Point out each malaria parasite.
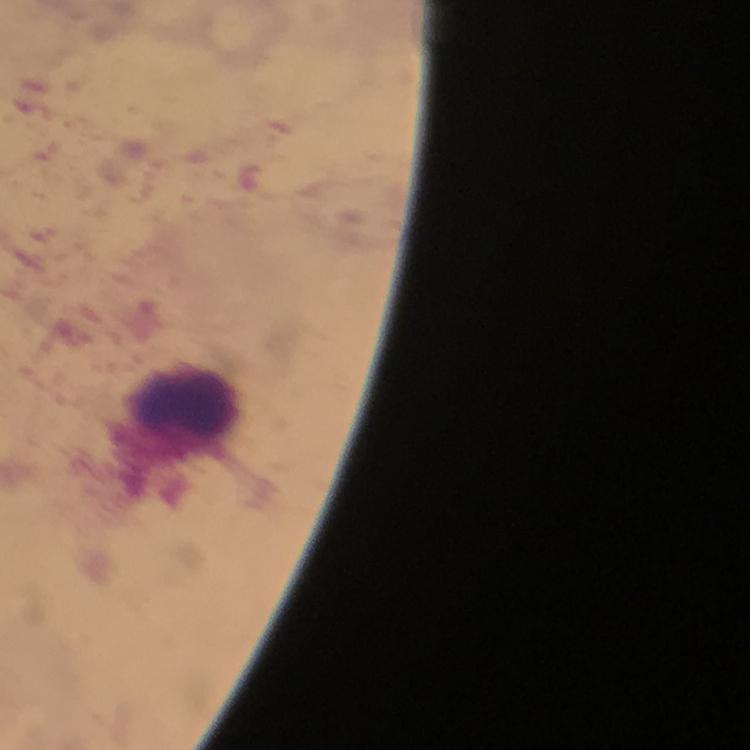
No malaria parasites detected.

Approximate centers as (x, y) in pixels. Leukocyte locations: (184, 403). Smartphone photograph taken through a microscope. A crop from one field of view. Image is 750×750 pixels. From a diagnostic examination for malaria. Thick blood film. Immersion oil was used. 100x magnification. Giemsa stain.